Comment on the morphology of the erythrocytes.
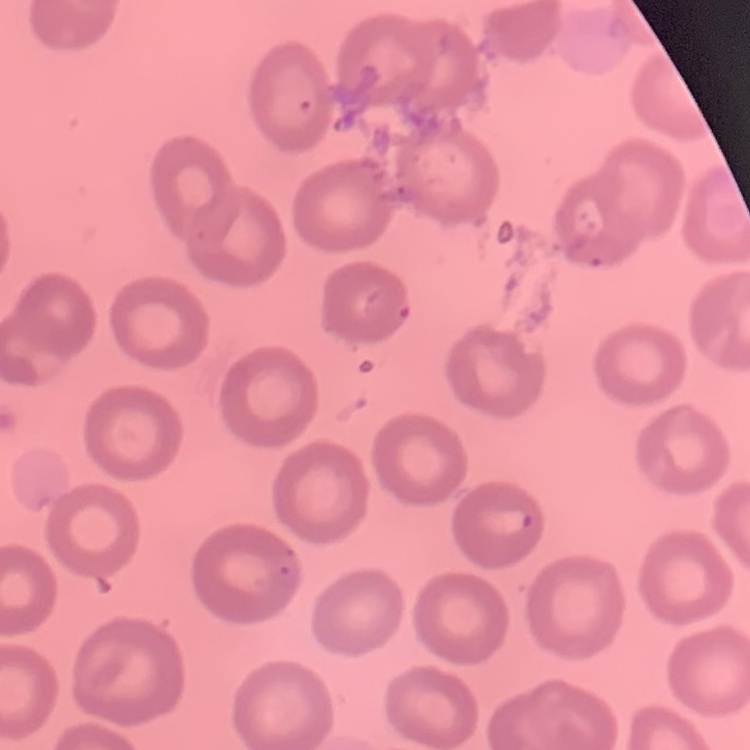

They show no rouleaux formation.

image type = square crop of a larger photomicrograph
stain = Field's or Giemsa
preparation = thin peripheral smear